Name the parasite shown.
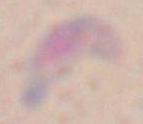

Toxoplasma gondii.

{
  "magnification": "1000x",
  "modality": "photomicrograph"
}